Classify this cell by malaria status.
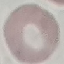

It is uninfected.

capture: smartphone camera at the microscope eyepiece
image_type: automatically extracted cell patch, resized to 64 × 64 pixels
preparation: thin blood film
stain: Giemsa